Name the parasite shown.
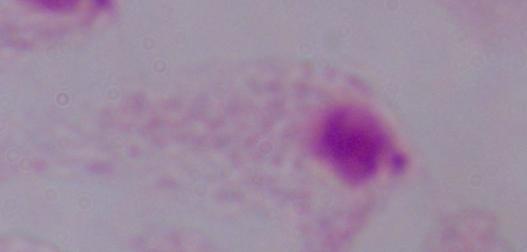

This is a trichomonad.

{
  "modality": "micrograph",
  "magnification": "1000x"
}